Locate every malaria parasite.
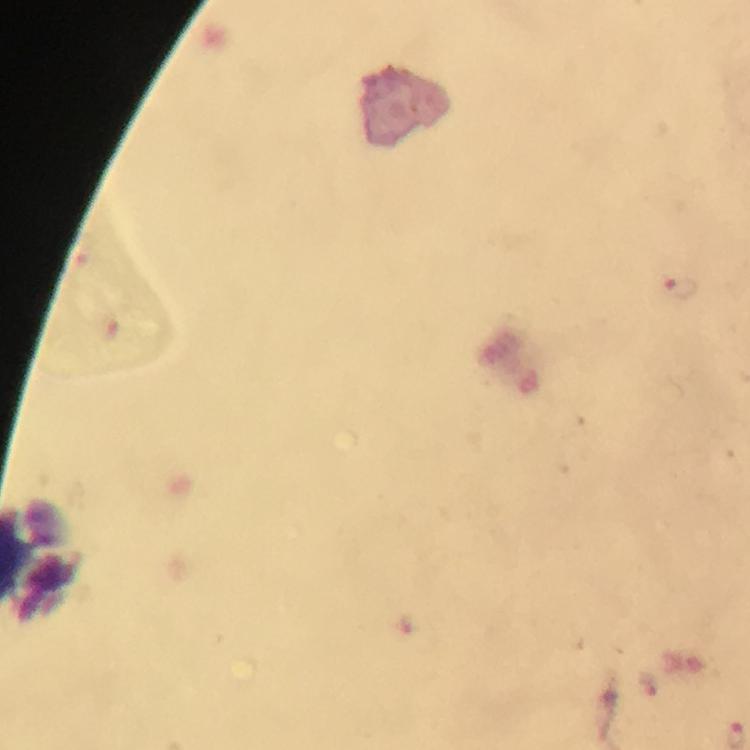

Approximate centers as (x, y) in pixels.
Malaria parasites: (681, 291), (645, 683).

magnification = 100x
image size = 750×750 pixels
preparation = thick blood film
capture = smartphone photograph through a microscope
context = from a diagnostic examination for malaria
stain = Giemsa
cropped from = one field of view
immersion oil = applied